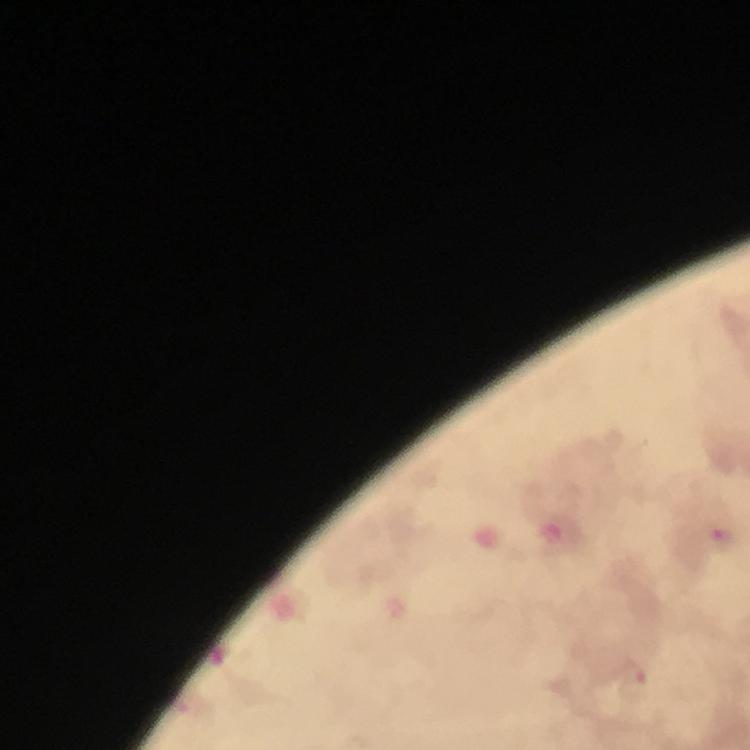

Approximate centers as {x, y} in pixels. Malaria parasite locations: {723, 535}, {634, 676}. At 100x magnification. Immersion oil applied. Image is 750×750 pixels. Cropped region of a single field of view. Giemsa-stained preparation. Photographed through the microscope with a smartphone camera. From a malaria diagnostic workup. Thick smear.